Give the position of every Plasmodium parasite.
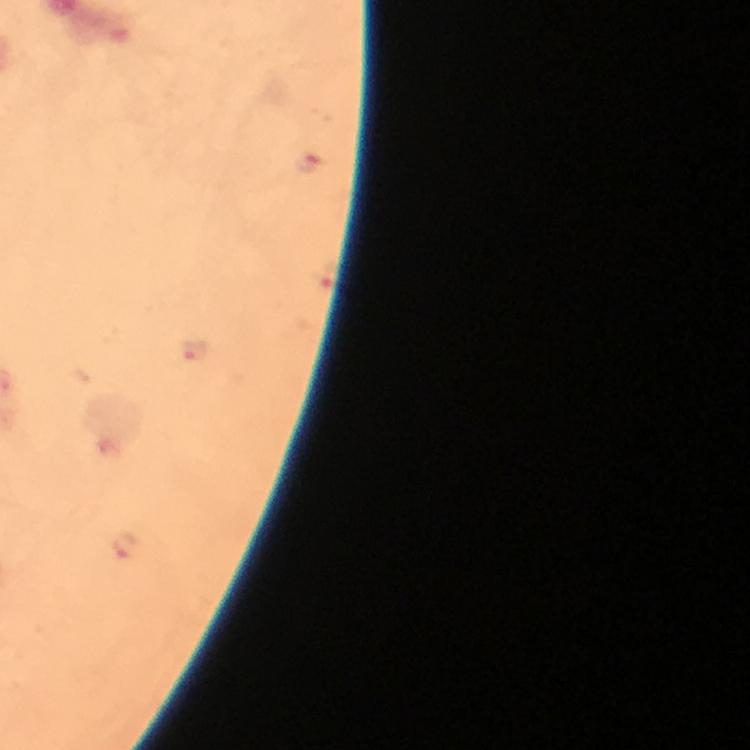

Approximate object centers, in pixels from the top-left corner.
Plasmodium parasites: (x=194, y=349), (x=126, y=546).

Summary:
  - Context: from a diagnostic examination for malaria
  - Preparation: thick smear
  - Immersion oil: applied
  - Cropped from: one field of view
  - Stain: Giemsa
  - Capture: smartphone camera through the microscope
  - Magnification: 100x
  - Image size: 750×750 pixels